Locate every Plasmodium parasite.
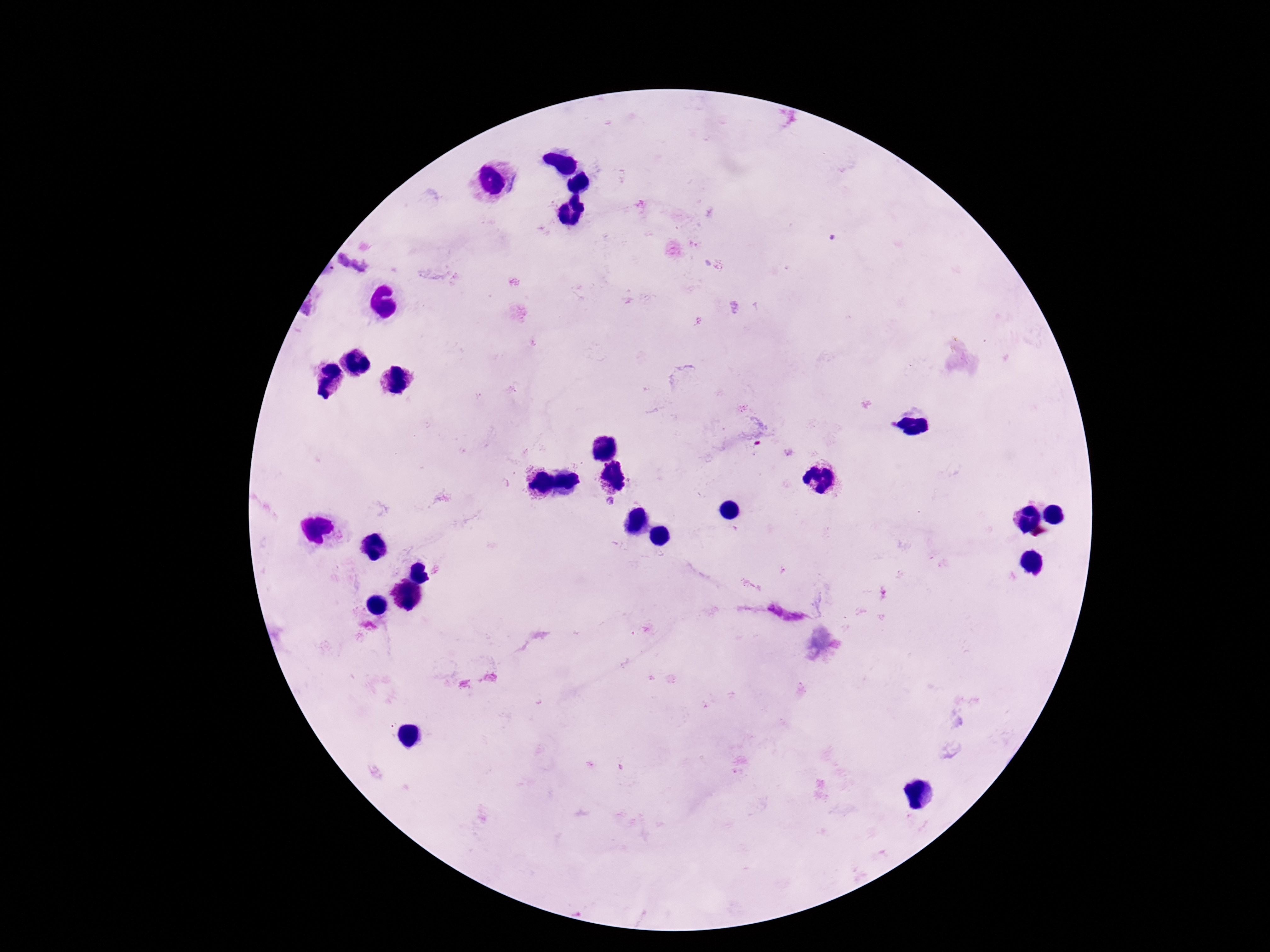
Approximate centers as (x, y) in pixels.
Plasmodium parasites: (610, 502), (775, 610).

Summary:
  - Preparation: thick blood film
  - Capture: smartphone camera through the microscope eyepiece
  - Image size: 1270×952 pixels
  - Patient malaria status: positive
  - Stain: Giemsa
  - Field of view: single
  - Magnification: 100x